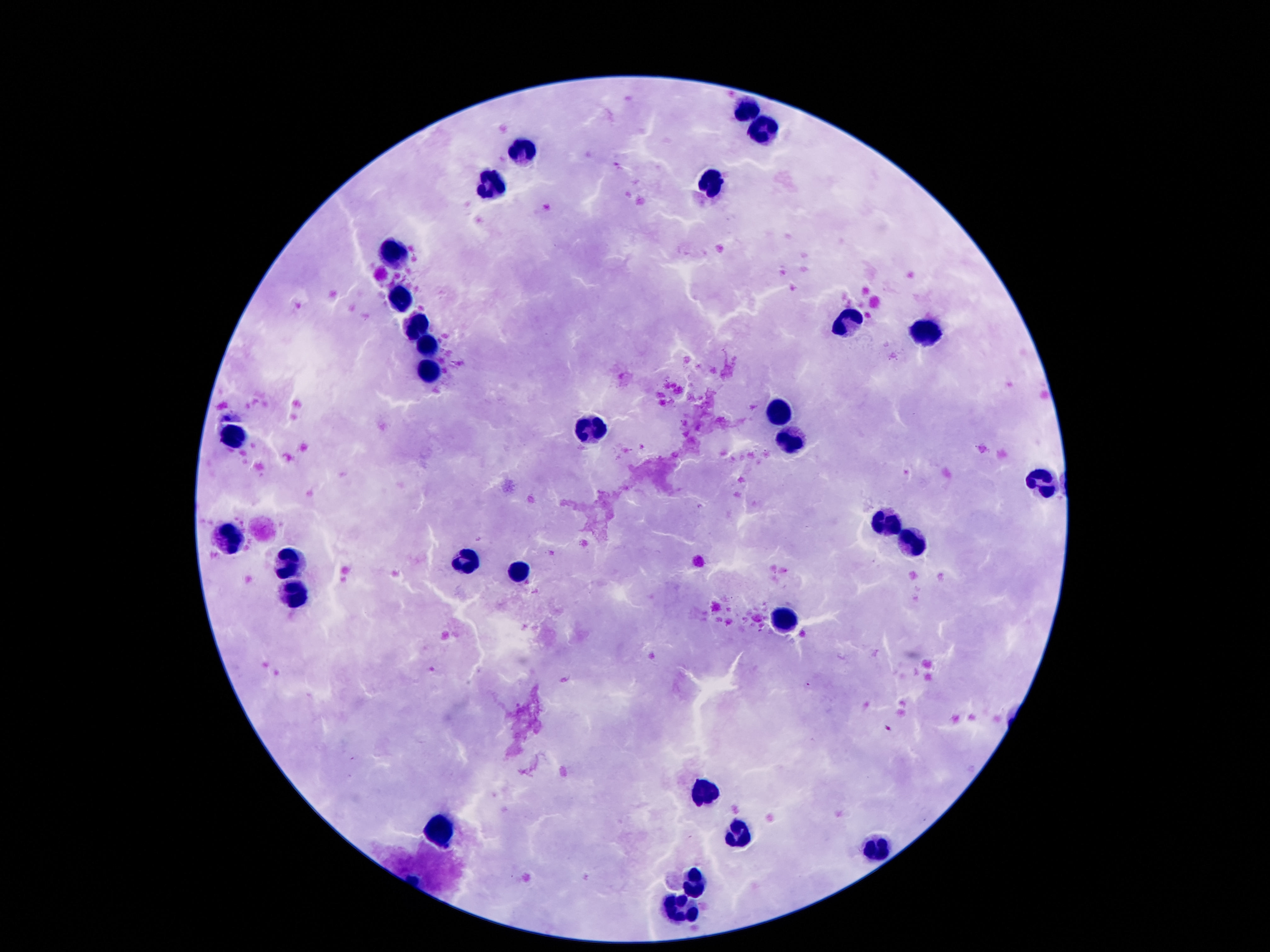

Approximate object centers, in pixels from the top-left corner. Leukocyte locations: (x=746, y=110), (x=767, y=130), (x=520, y=148), (x=709, y=182), (x=495, y=187), (x=396, y=256), (x=403, y=299), (x=849, y=321), (x=418, y=325), (x=923, y=331), (x=429, y=345), (x=431, y=372), (x=779, y=413), (x=592, y=433), (x=236, y=436), (x=793, y=441), (x=1045, y=482), (x=888, y=523), (x=228, y=535), (x=916, y=540), (x=287, y=561), (x=466, y=561), (x=518, y=569), (x=292, y=589), (x=788, y=622), (x=706, y=790), (x=439, y=832), (x=741, y=834), (x=875, y=846), (x=697, y=883), (x=679, y=912). Photographed through the microscope eyepiece with a smartphone camera. Giemsa stain. Thick blood smear. Image is 1270×952 pixels. One field from this slide. 100x magnification. Patient malaria status: not infected.